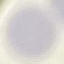

Malaria status: uninfected. Photographed with a smartphone camera at the microscope eyepiece. Giemsa-stained preparation. Automatically extracted cell patch, resized to 64 × 64 pixels. Thin smear of blood.